Locate and identify every blood parasite.
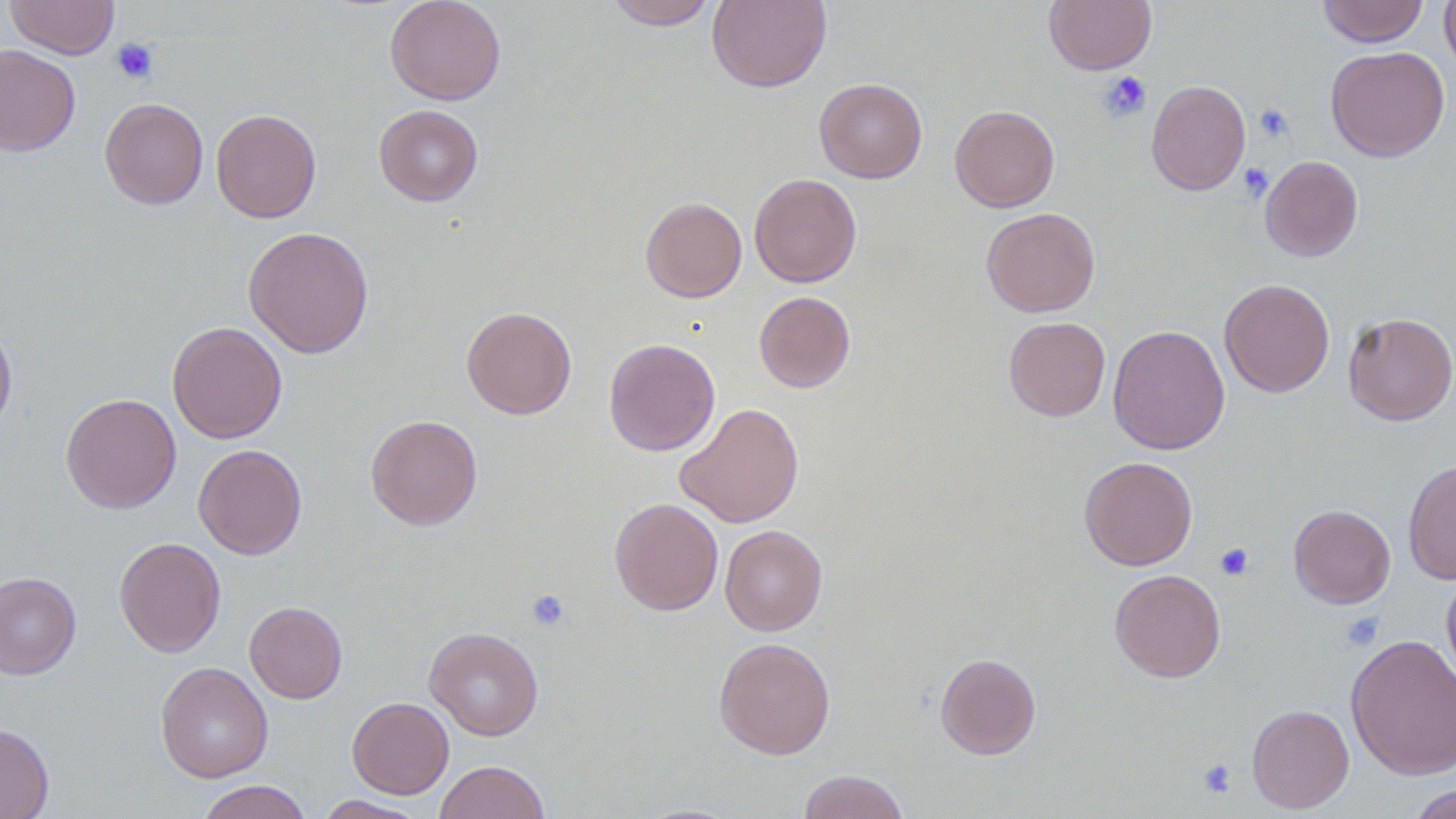
No blood parasites seen.

Approximate bounding boxes as named x1/y1/x2/y2 corners in pixels. Platelet locations: (x1=112, y1=38, x2=158, y2=84), (x1=1099, y1=71, x2=1153, y2=122), (x1=1254, y1=104, x2=1294, y2=142), (x1=1238, y1=162, x2=1274, y2=201), (x1=1215, y1=543, x2=1254, y2=580), (x1=526, y1=588, x2=571, y2=632), (x1=1342, y1=612, x2=1384, y2=650), (x1=1197, y1=758, x2=1237, y2=798). Uninfected red blood cell locations: (x1=5, y1=0, x2=119, y2=59), (x1=384, y1=0, x2=506, y2=105), (x1=604, y1=0, x2=718, y2=29), (x1=707, y1=0, x2=832, y2=92), (x1=1044, y1=0, x2=1156, y2=74), (x1=1317, y1=0, x2=1429, y2=47), (x1=1439, y1=0, x2=1456, y2=79), (x1=0, y1=44, x2=81, y2=156), (x1=1325, y1=46, x2=1450, y2=162), (x1=814, y1=78, x2=928, y2=183), (x1=1146, y1=79, x2=1251, y2=196), (x1=99, y1=97, x2=208, y2=209), (x1=374, y1=104, x2=483, y2=206), (x1=950, y1=105, x2=1060, y2=213), (x1=211, y1=108, x2=321, y2=223), (x1=1259, y1=156, x2=1363, y2=262), (x1=749, y1=173, x2=862, y2=288), (x1=640, y1=197, x2=747, y2=302), (x1=981, y1=207, x2=1100, y2=316), (x1=243, y1=225, x2=374, y2=359), (x1=1219, y1=278, x2=1335, y2=397), (x1=754, y1=291, x2=856, y2=393), (x1=461, y1=306, x2=577, y2=419), (x1=1343, y1=312, x2=1456, y2=426), (x1=1004, y1=316, x2=1110, y2=421), (x1=0, y1=318, x2=17, y2=437), (x1=167, y1=322, x2=288, y2=444), (x1=1107, y1=325, x2=1230, y2=455), (x1=604, y1=338, x2=720, y2=456), (x1=60, y1=393, x2=181, y2=514), (x1=675, y1=402, x2=804, y2=528), (x1=365, y1=414, x2=483, y2=530), (x1=193, y1=444, x2=307, y2=560), (x1=1079, y1=456, x2=1198, y2=571), (x1=1403, y1=460, x2=1456, y2=584), (x1=609, y1=497, x2=723, y2=615), (x1=1288, y1=504, x2=1395, y2=608), (x1=720, y1=525, x2=828, y2=636), (x1=114, y1=537, x2=227, y2=657), (x1=1109, y1=568, x2=1226, y2=682), (x1=0, y1=571, x2=81, y2=679), (x1=1441, y1=571, x2=1456, y2=688), (x1=245, y1=601, x2=347, y2=704), (x1=424, y1=627, x2=544, y2=740), (x1=1345, y1=633, x2=1456, y2=780), (x1=713, y1=637, x2=836, y2=759), (x1=935, y1=652, x2=1041, y2=760), (x1=155, y1=661, x2=273, y2=783), (x1=346, y1=696, x2=454, y2=799), (x1=1247, y1=704, x2=1354, y2=813), (x1=0, y1=723, x2=54, y2=819), (x1=434, y1=760, x2=551, y2=819), (x1=797, y1=770, x2=910, y2=819), (x1=194, y1=780, x2=313, y2=819), (x1=1405, y1=783, x2=1455, y2=818), (x1=313, y1=795, x2=430, y2=818). Slide-level diagnosis: negative for blood parasites. Thin blood film. Optical microscopy. Captured at 1000x magnification. Image is 1456×819 pixels. One field of a larger specimen.